Locate every Plasmodium parasite.
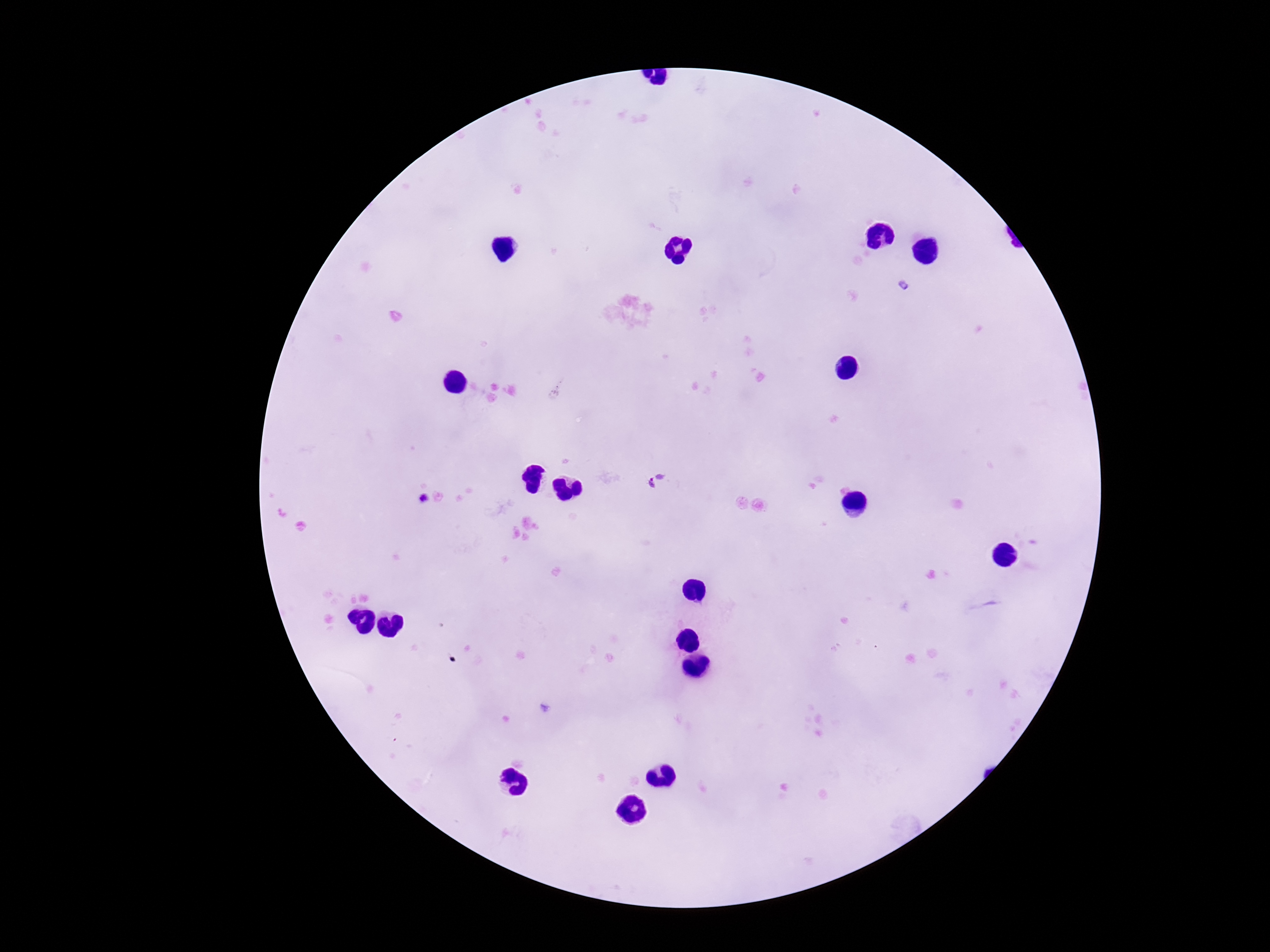

Approximate centers as [x, y] in pixels.
Plasmodium parasites: [655, 481], [420, 500].

One field from this slide. Giemsa-stained preparation. Image is 1270×952 pixels. Thick peripheral-blood smear. Patient malaria status: infected. 100x magnification. Photographed through the microscope eyepiece with a smartphone camera.